Classify this cell by malaria status.
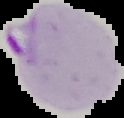

Parasitized.

preparation = thin blood film
image size = 124×118 pixels
image type = segmented cell region on a black background